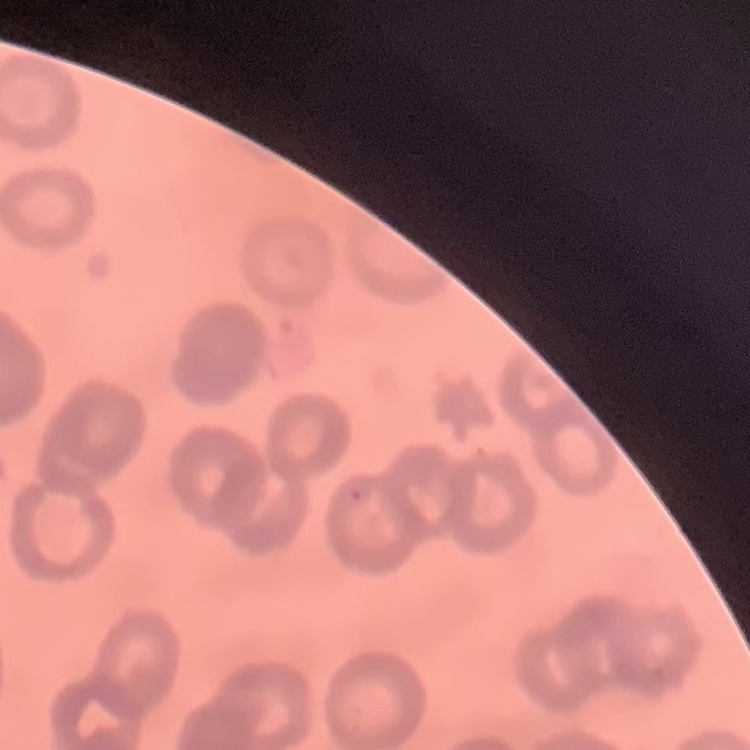
The red blood cells exhibit rouleaux formation. Field's or Giemsa stain. Thin peripheral smear. Square crop of a larger photomicrograph.